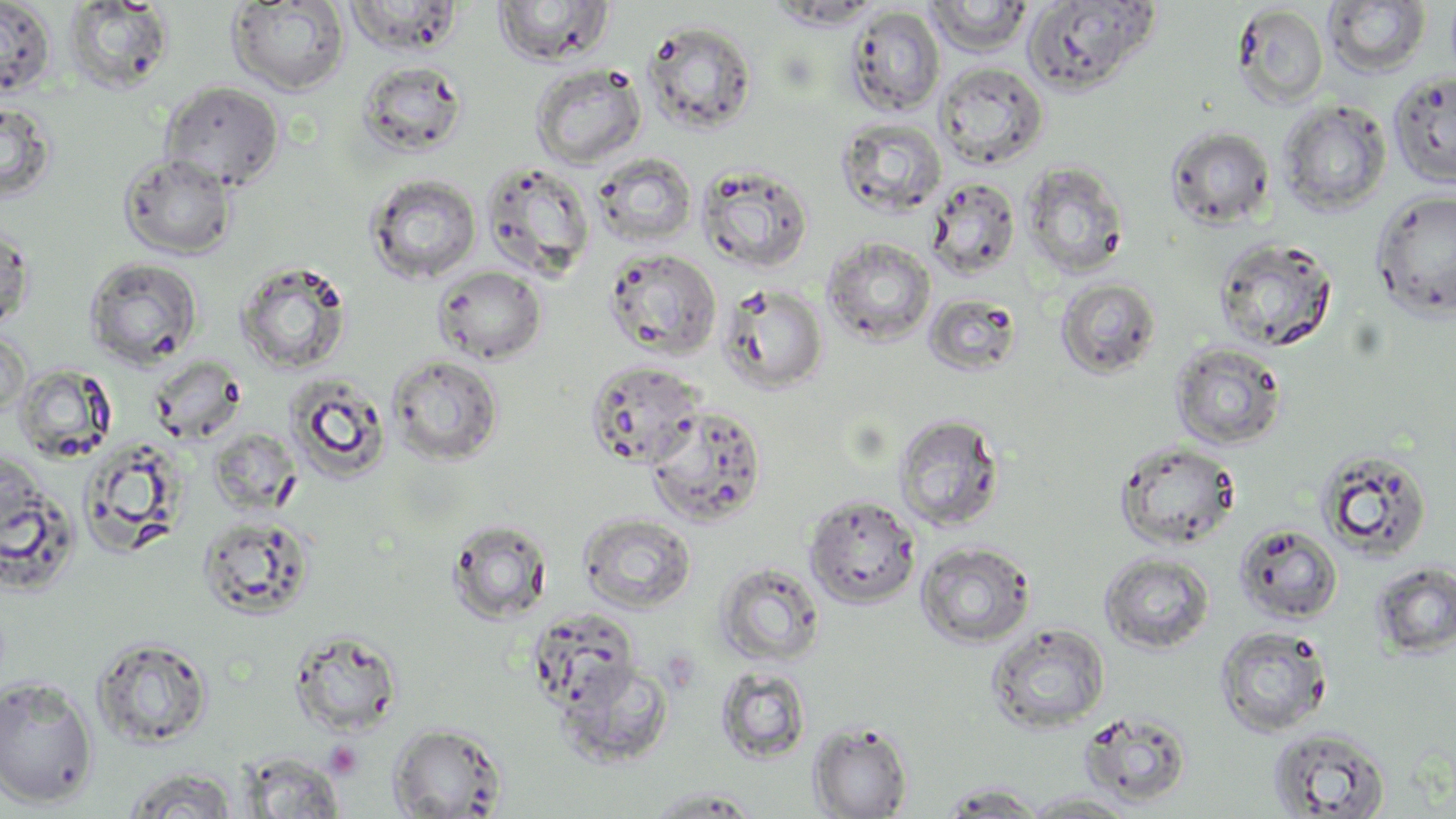

Summary:
  - Coordinate format: approximate bounding boxes as named x1/y1/x2/y2 corners in pixels
  - Uninfected red blood cell locations: (x1=0, y1=0, x2=56, y2=98), (x1=343, y1=0, x2=465, y2=56), (x1=492, y1=0, x2=615, y2=67), (x1=1022, y1=0, x2=1160, y2=96), (x1=62, y1=1, x2=175, y2=94), (x1=226, y1=1, x2=350, y2=96), (x1=767, y1=1, x2=885, y2=30), (x1=925, y1=1, x2=1035, y2=56), (x1=1324, y1=1, x2=1431, y2=78), (x1=1232, y1=3, x2=1329, y2=110), (x1=845, y1=5, x2=945, y2=117), (x1=642, y1=20, x2=758, y2=135), (x1=355, y1=60, x2=468, y2=159), (x1=935, y1=61, x2=1049, y2=171), (x1=529, y1=63, x2=648, y2=170), (x1=1388, y1=71, x2=1456, y2=189), (x1=159, y1=80, x2=285, y2=192), (x1=0, y1=97, x2=58, y2=205), (x1=1278, y1=99, x2=1392, y2=216), (x1=836, y1=117, x2=947, y2=218), (x1=1165, y1=126, x2=1275, y2=230), (x1=117, y1=152, x2=239, y2=261), (x1=592, y1=153, x2=698, y2=249), (x1=479, y1=160, x2=596, y2=282), (x1=1021, y1=160, x2=1130, y2=279), (x1=697, y1=163, x2=815, y2=274), (x1=365, y1=173, x2=482, y2=285), (x1=925, y1=177, x2=1021, y2=280), (x1=1371, y1=188, x2=1456, y2=320), (x1=1, y1=220, x2=35, y2=335), (x1=822, y1=236, x2=937, y2=347), (x1=1213, y1=237, x2=1338, y2=353), (x1=602, y1=248, x2=722, y2=360), (x1=83, y1=256, x2=204, y2=370), (x1=235, y1=259, x2=353, y2=375), (x1=432, y1=265, x2=548, y2=365), (x1=1056, y1=277, x2=1161, y2=380), (x1=718, y1=281, x2=829, y2=394), (x1=922, y1=293, x2=1022, y2=378), (x1=0, y1=327, x2=31, y2=421), (x1=1171, y1=341, x2=1287, y2=450), (x1=387, y1=353, x2=505, y2=467), (x1=147, y1=355, x2=248, y2=446), (x1=584, y1=359, x2=707, y2=469), (x1=11, y1=364, x2=119, y2=466), (x1=283, y1=373, x2=392, y2=485), (x1=645, y1=404, x2=768, y2=527), (x1=893, y1=413, x2=1005, y2=532), (x1=78, y1=436, x2=190, y2=556), (x1=1113, y1=439, x2=1241, y2=551), (x1=1314, y1=447, x2=1434, y2=562), (x1=1, y1=452, x2=74, y2=593), (x1=804, y1=492, x2=921, y2=609), (x1=577, y1=512, x2=697, y2=613), (x1=196, y1=514, x2=316, y2=620), (x1=446, y1=518, x2=553, y2=624), (x1=1234, y1=524, x2=1344, y2=625), (x1=916, y1=541, x2=1036, y2=649), (x1=1099, y1=552, x2=1214, y2=654), (x1=1372, y1=561, x2=1456, y2=658), (x1=714, y1=562, x2=825, y2=667), (x1=527, y1=607, x2=642, y2=710), (x1=986, y1=623, x2=1111, y2=735), (x1=1214, y1=626, x2=1332, y2=738), (x1=290, y1=629, x2=405, y2=737), (x1=90, y1=635, x2=215, y2=750), (x1=557, y1=658, x2=675, y2=766), (x1=714, y1=666, x2=812, y2=765), (x1=0, y1=674, x2=99, y2=809), (x1=1078, y1=709, x2=1194, y2=807), (x1=388, y1=722, x2=508, y2=818), (x1=808, y1=722, x2=913, y2=819), (x1=1267, y1=726, x2=1393, y2=818), (x1=240, y1=753, x2=346, y2=818), (x1=120, y1=768, x2=241, y2=818), (x1=936, y1=782, x2=1048, y2=816), (x1=643, y1=786, x2=764, y2=817), (x1=1022, y1=791, x2=1139, y2=817)
  - Platelet locations: (x1=323, y1=741, x2=363, y2=780)
  - Slide-level diagnosis: no evidence of blood parasites
  - Preparation: thin blood film
  - Modality: optical microscopy
  - Image size: 1456×819 pixels
  - Stain: May-Grünwald-Giemsa
  - Magnification: 1000x
  - Field of view: single